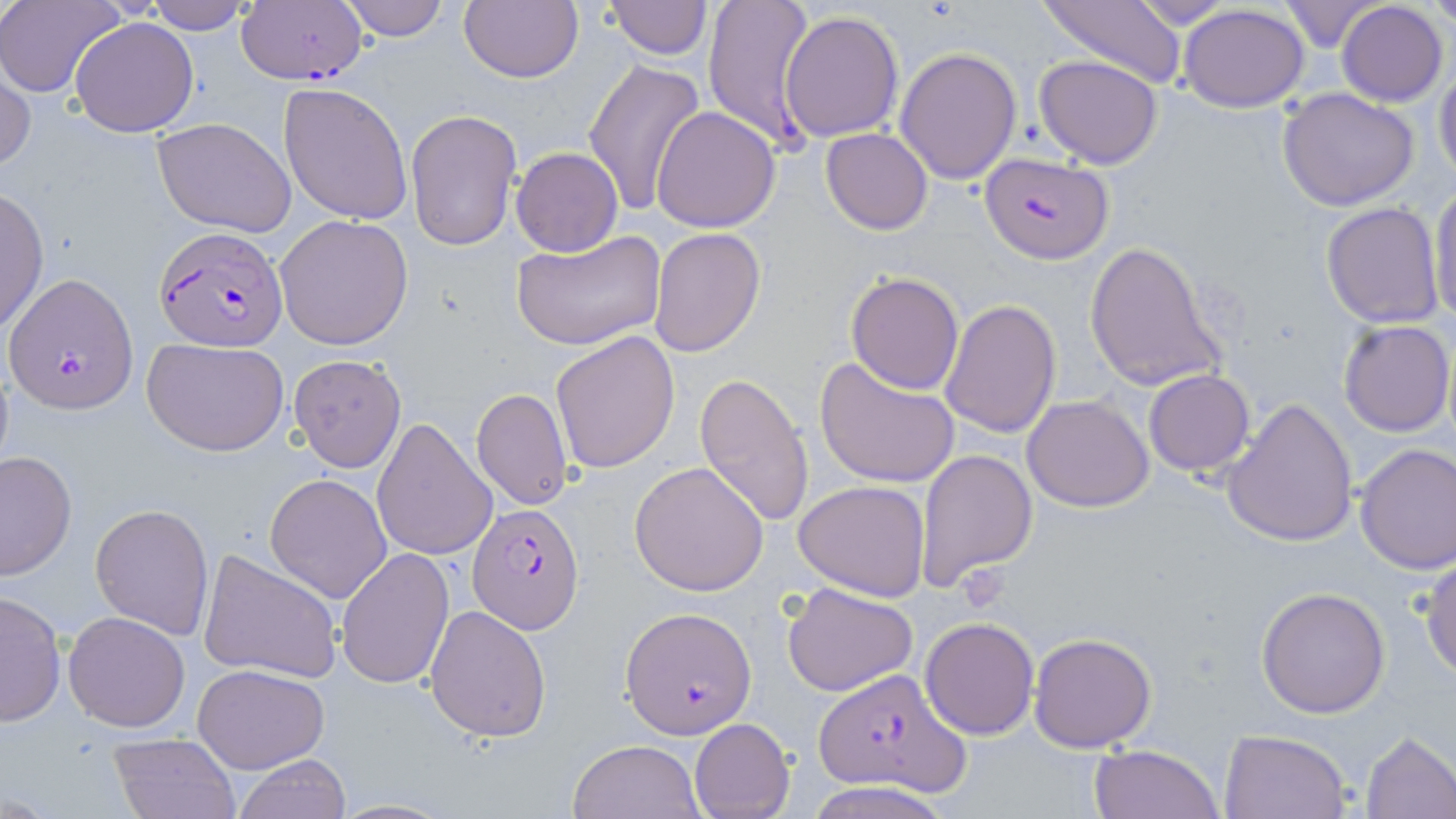
Summary:
  - Coordinate format: approximate bounding boxes as (x1,y1)-(x2,y2) corner pairs in pixels
  - Platelet locations: (955,566)-(1010,612)
  - Plasmodium falciparum-infected red blood cell locations: (235,0)-(368,87), (979,153)-(1113,265), (155,226)-(286,353), (4,274)-(137,414), (464,502)-(583,634), (620,608)-(756,738), (812,669)-(969,795)
  - Uninfected red blood cell locations: (2,0)-(125,98), (147,0)-(255,33), (338,0)-(453,42), (459,0)-(583,83), (604,0)-(711,58), (703,0)-(818,149), (1039,0)-(1187,88), (1428,0)-(1456,31), (1125,1)-(1241,28), (1278,1)-(1384,53), (1336,1)-(1447,107), (1178,5)-(1310,111), (780,8)-(905,142), (69,17)-(199,137), (895,45)-(1022,183), (1034,54)-(1163,169), (582,57)-(707,217), (1,60)-(35,173), (1433,63)-(1456,186), (278,81)-(413,225), (1277,87)-(1421,211), (650,106)-(780,232), (405,108)-(521,250), (152,117)-(298,239), (821,129)-(932,235), (511,147)-(623,257), (1428,184)-(1456,328), (0,187)-(49,337), (1320,202)-(1445,328), (275,214)-(413,350), (650,227)-(765,357), (512,230)-(667,353), (1084,240)-(1227,393), (846,271)-(964,393), (940,298)-(1062,438), (1337,318)-(1454,437), (549,330)-(679,474), (141,336)-(291,457), (813,354)-(960,490), (288,355)-(407,474), (1143,369)-(1256,477), (693,372)-(815,525), (472,388)-(573,509), (1022,395)-(1155,511), (1222,396)-(1358,548), (370,417)-(496,562), (1355,442)-(1456,573), (916,447)-(1038,593), (0,449)-(76,582), (629,460)-(770,595), (265,474)-(392,603), (793,479)-(931,601), (89,502)-(213,638), (336,547)-(454,690), (198,548)-(343,683), (1421,553)-(1456,679), (783,581)-(917,697), (1256,586)-(1388,719), (1,590)-(66,726), (424,604)-(551,742), (63,610)-(192,731), (919,616)-(1039,739), (1028,632)-(1158,753), (192,663)-(330,773), (689,718)-(794,819), (1219,728)-(1350,819), (1359,731)-(1456,817), (108,733)-(239,819), (567,738)-(706,819), (1090,743)-(1225,819), (232,756)-(352,819), (804,781)-(957,819)
  - Slide-level diagnosis: Plasmodium falciparum
  - Field of view: single
  - Magnification: 1000x
  - Image size: 1456×819 pixels
  - Stain: May-Grünwald-Giemsa
  - Preparation: thin blood film
  - Modality: optical microscopy